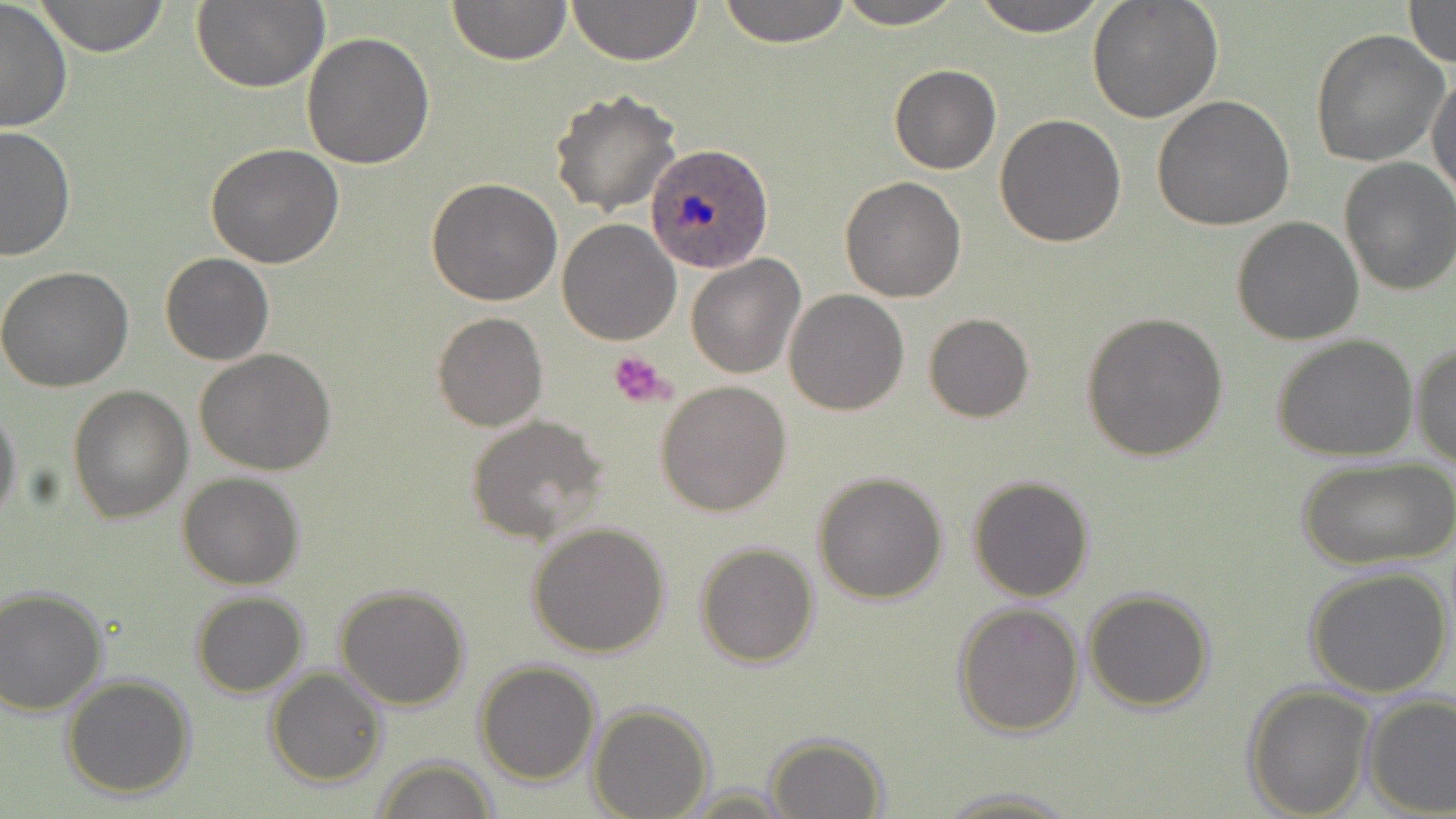
Approximate bounding boxes as named x1/y1/x2/y2 corners in pixels. Platelet locations: (x1=608, y1=351, x2=678, y2=409). Uninfected red blood cell locations: (x1=34, y1=0, x2=170, y2=56), (x1=446, y1=0, x2=570, y2=65), (x1=567, y1=0, x2=702, y2=66), (x1=717, y1=0, x2=853, y2=47), (x1=831, y1=0, x2=969, y2=28), (x1=968, y1=0, x2=1114, y2=36), (x1=1085, y1=0, x2=1224, y2=122), (x1=1401, y1=0, x2=1456, y2=69), (x1=0, y1=1, x2=74, y2=134), (x1=190, y1=1, x2=329, y2=92), (x1=1309, y1=28, x2=1450, y2=168), (x1=302, y1=30, x2=434, y2=170), (x1=888, y1=64, x2=1001, y2=176), (x1=1428, y1=68, x2=1456, y2=202), (x1=549, y1=88, x2=682, y2=214), (x1=1152, y1=93, x2=1297, y2=231), (x1=995, y1=114, x2=1127, y2=248), (x1=0, y1=124, x2=74, y2=260), (x1=205, y1=142, x2=345, y2=268), (x1=1338, y1=158, x2=1456, y2=296), (x1=427, y1=176, x2=562, y2=305), (x1=839, y1=176, x2=967, y2=303), (x1=1230, y1=217, x2=1364, y2=345), (x1=558, y1=220, x2=681, y2=345), (x1=159, y1=252, x2=273, y2=366), (x1=686, y1=255, x2=805, y2=379), (x1=0, y1=267, x2=133, y2=391), (x1=784, y1=290, x2=909, y2=414), (x1=1079, y1=311, x2=1229, y2=461), (x1=432, y1=313, x2=548, y2=431), (x1=923, y1=313, x2=1034, y2=424), (x1=1271, y1=334, x2=1420, y2=463), (x1=1411, y1=340, x2=1456, y2=472), (x1=194, y1=348, x2=339, y2=476), (x1=656, y1=380, x2=791, y2=516), (x1=67, y1=386, x2=193, y2=523), (x1=0, y1=402, x2=21, y2=525), (x1=464, y1=415, x2=609, y2=546), (x1=1296, y1=455, x2=1453, y2=570), (x1=812, y1=471, x2=949, y2=605), (x1=177, y1=472, x2=305, y2=589), (x1=967, y1=475, x2=1096, y2=602), (x1=526, y1=521, x2=671, y2=659), (x1=695, y1=542, x2=819, y2=667), (x1=1303, y1=564, x2=1455, y2=701), (x1=0, y1=584, x2=109, y2=716), (x1=334, y1=584, x2=470, y2=710), (x1=1083, y1=587, x2=1215, y2=713), (x1=191, y1=590, x2=309, y2=697), (x1=952, y1=600, x2=1085, y2=738), (x1=476, y1=660, x2=601, y2=785), (x1=266, y1=666, x2=387, y2=787), (x1=60, y1=673, x2=197, y2=800), (x1=1243, y1=682, x2=1372, y2=817), (x1=1360, y1=692, x2=1456, y2=817), (x1=588, y1=703, x2=714, y2=819), (x1=763, y1=733, x2=889, y2=818), (x1=371, y1=756, x2=499, y2=819), (x1=930, y1=785, x2=1085, y2=817). Plasmodium ovale-infected red blood cell locations: (x1=649, y1=144, x2=774, y2=273). Slide-level diagnosis: Plasmodium ovale. Image is 1456×819 pixels. Single field of view. Captured at 1000x magnification. Light microscopy. May-Grünwald-Giemsa-stained preparation. Thin blood film.